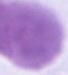

{
  "modality": "photomicrograph",
  "identification": "red blood cell",
  "magnification": "1000x"
}